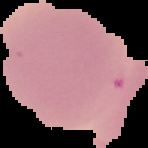

From a thin blood film. The area outside the segmented cell region is set to black. Result: negative for Plasmodium parasites. Image is 148×148 pixels.